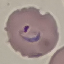
{
  "malaria_status": "parasitized",
  "image_type": "automatically extracted cell patch, resized to 64 × 64 pixels",
  "preparation": "thin blood film",
  "capture": "smartphone through the microscope eyepiece",
  "stain": "Giemsa"
}